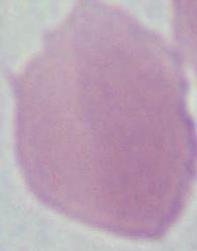

identification: red blood cell
magnification: 1000x
modality: photomicrograph